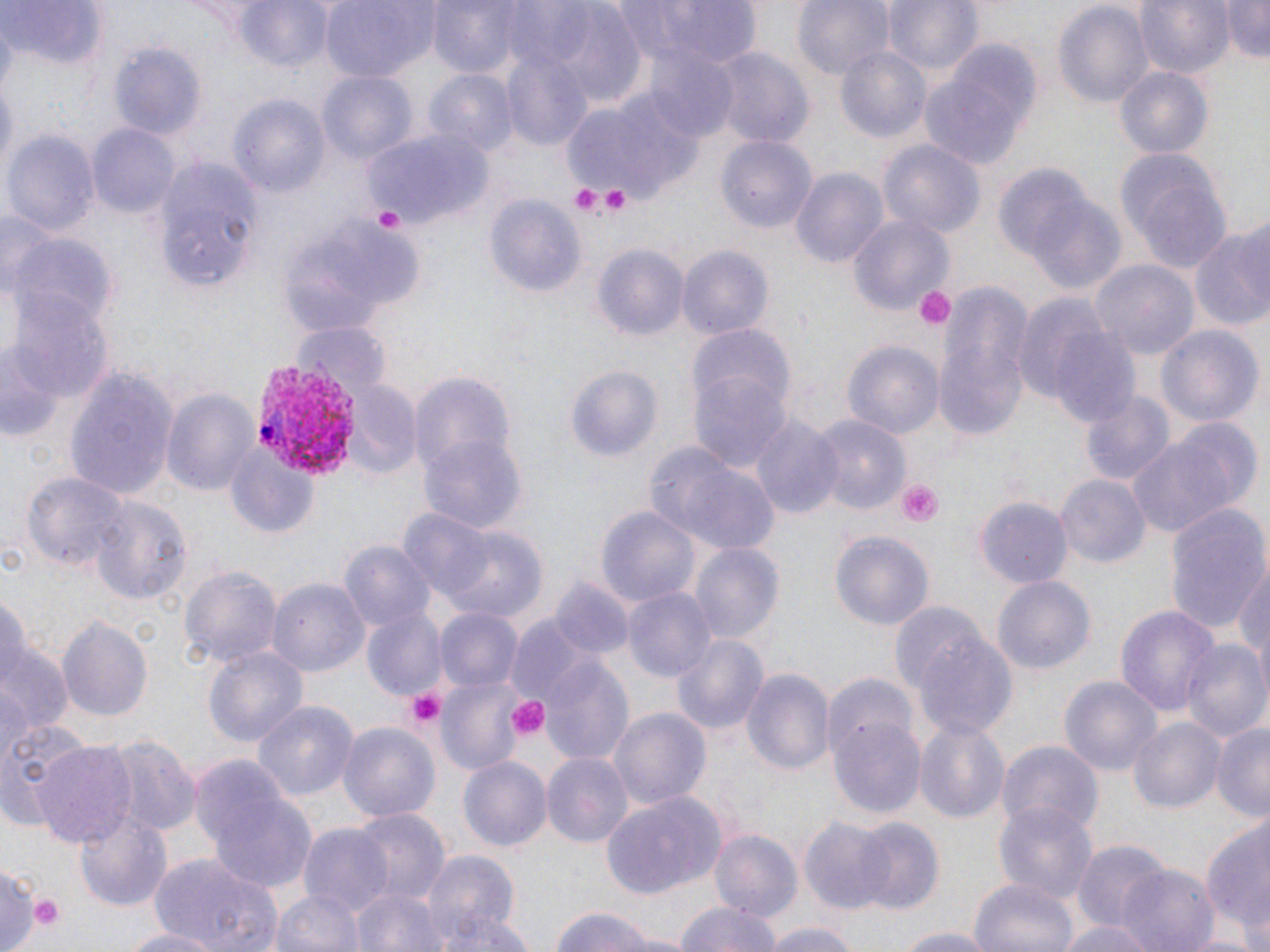
Summary:
  - Coordinate format: approximate bounding boxes as (x1,y1)-(x2,y2) corner pairs in pixels
  - Plasmodium vivax-infected red blood cell locations: (250,361)-(367,480)
  - Platelet locations: (570,183)-(605,218), (595,184)-(635,215), (371,204)-(406,233), (914,285)-(955,331), (896,478)-(945,529), (404,687)-(446,729), (507,694)-(550,744), (26,891)-(65,934)
  - Uninfected red blood cell locations: (234,0)-(335,74), (319,0)-(431,84), (427,0)-(530,79), (616,0)-(760,68), (793,0)-(894,83), (882,0)-(982,79), (1133,0)-(1234,81), (1218,0)-(1270,62), (1054,1)-(1153,112), (1,3)-(106,74), (542,7)-(648,106), (109,40)-(207,140), (916,41)-(1043,174), (834,44)-(933,146), (706,45)-(816,149), (645,52)-(740,143), (503,59)-(593,152), (1116,65)-(1214,160), (426,67)-(518,159), (318,71)-(417,166), (228,90)-(331,198), (559,95)-(698,200), (88,123)-(180,220), (3,128)-(100,237), (363,130)-(493,226), (717,136)-(815,237), (878,139)-(984,238), (1115,146)-(1231,273), (159,159)-(258,255), (991,161)-(1109,279), (792,167)-(887,270), (1022,192)-(1129,296), (486,193)-(586,294), (164,208)-(249,288), (850,213)-(953,318), (1189,225)-(1270,335), (7,228)-(114,332), (593,245)-(690,344), (676,246)-(774,343), (1091,261)-(1199,363), (933,281)-(1034,443), (7,288)-(113,407), (1011,292)-(1131,416), (294,321)-(390,394), (1157,325)-(1263,430), (1051,327)-(1144,429), (688,329)-(794,424), (844,340)-(945,445), (1,346)-(61,442), (564,364)-(663,462), (689,367)-(792,476), (67,368)-(176,499), (407,372)-(515,473), (342,379)-(419,479), (163,387)-(261,500), (1081,390)-(1174,485), (811,413)-(910,514), (749,414)-(844,520), (1164,418)-(1264,517), (421,436)-(525,537), (1125,436)-(1241,539), (648,443)-(783,554), (227,449)-(319,538), (24,469)-(127,576), (1057,474)-(1151,570), (89,493)-(192,608), (976,495)-(1073,591), (1163,503)-(1270,638), (399,506)-(498,603), (595,507)-(699,608), (446,529)-(547,623), (830,531)-(934,631), (339,541)-(436,634), (689,542)-(784,645), (1232,560)-(1270,667), (180,564)-(282,672), (992,575)-(1096,675), (553,576)-(634,661), (268,577)-(369,678), (623,585)-(717,683), (0,593)-(31,687), (362,604)-(447,699), (1116,604)-(1220,722), (436,609)-(519,693), (57,617)-(152,720), (505,618)-(593,707), (672,633)-(767,736), (912,633)-(1020,741), (2,639)-(72,733), (1182,641)-(1270,744), (202,643)-(309,750), (539,653)-(634,766), (742,669)-(834,779), (820,671)-(915,759), (1058,674)-(1163,779), (438,675)-(528,776), (0,681)-(33,766), (252,699)-(357,802), (608,707)-(710,812), (1131,716)-(1226,814), (830,719)-(927,820), (0,720)-(94,829), (1213,720)-(1270,822), (339,722)-(439,825), (913,722)-(1010,827), (100,733)-(199,837), (31,741)-(136,844), (998,741)-(1103,838), (544,754)-(632,848), (458,757)-(552,853), (551,764)-(684,868), (201,773)-(318,896), (600,789)-(729,900), (992,802)-(1099,905), (74,806)-(175,909), (350,808)-(448,904), (801,815)-(891,915), (850,817)-(944,913), (1200,823)-(1270,935), (299,824)-(394,917), (711,830)-(802,922), (1073,841)-(1169,933), (422,850)-(517,948), (147,852)-(284,952), (1119,863)-(1221,952), (969,877)-(1076,952), (353,883)-(442,952), (271,892)-(361,952), (673,899)-(786,952), (549,905)-(667,952), (435,912)-(534,952), (1058,917)-(1156,952), (759,921)-(867,952), (117,925)-(227,952), (886,926)-(1002,951)
  - Slide-level diagnosis: Plasmodium vivax
  - Modality: optical microscopy
  - Image size: 1270×952 pixels
  - Field of view: one of a larger specimen
  - Stain: May-Grünwald-Giemsa
  - Magnification: 1000x
  - Preparation: thin blood smear